Classify this cell by malaria status.
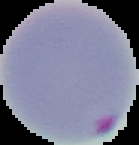

Parasitized.

{
  "preparation": "thin blood smear",
  "image_type": "segmented cell region on a black background",
  "image_size": "139×145 pixels"
}